Locate every Plasmodium parasite and identify its life-cycle stage.
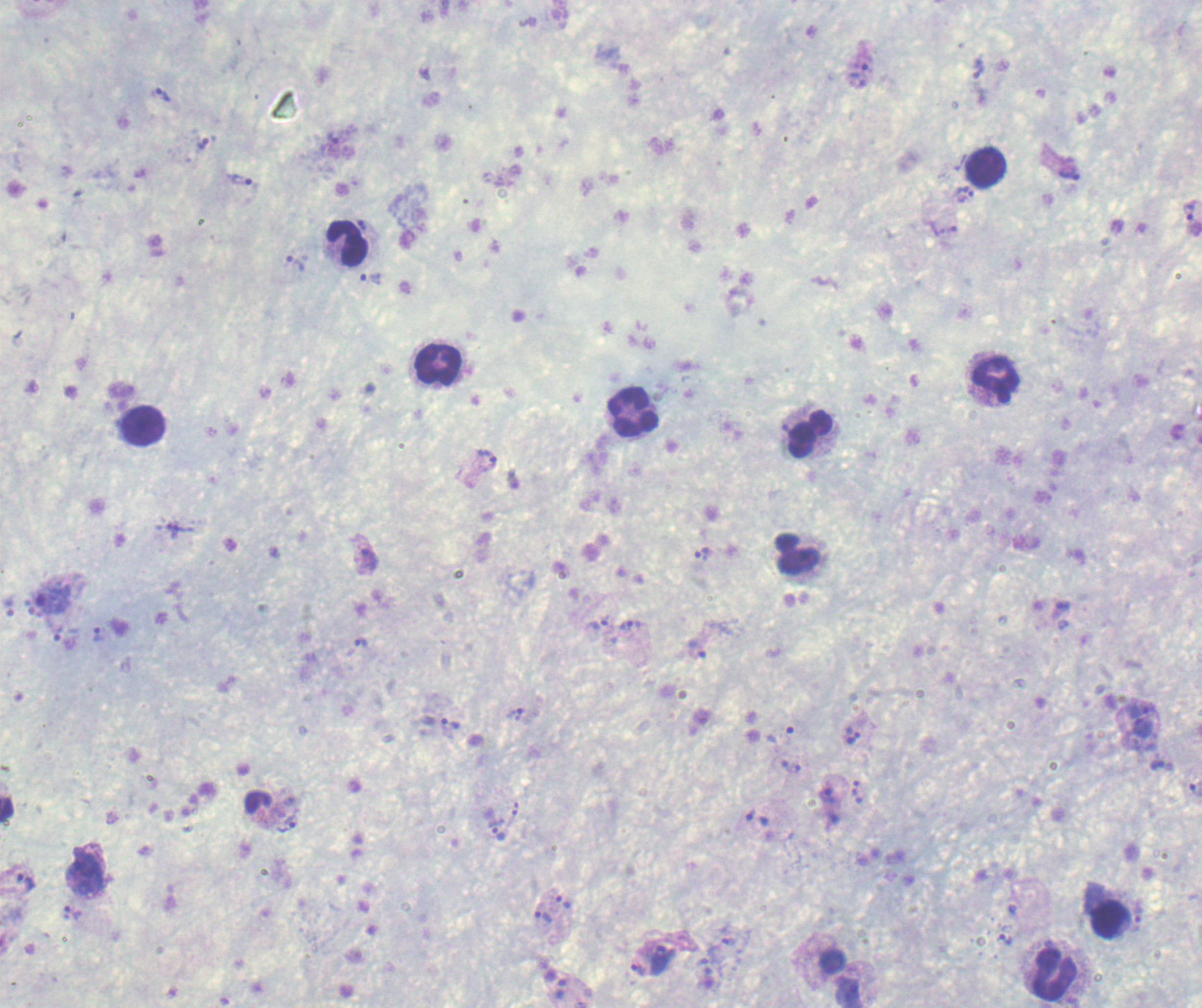

Approximate centers as (x, y) in pixels.
Trophozoites: (979, 68), (857, 75), (163, 95), (333, 137), (202, 144), (1069, 173), (240, 178), (964, 192), (1189, 212), (943, 228), (296, 263), (371, 278), (486, 461), (172, 529), (702, 552), (366, 561), (1061, 610), (598, 624), (627, 627), (99, 634), (360, 642), (697, 649), (1140, 710), (515, 714), (451, 724), (1141, 728), (852, 734), (780, 735), (1157, 764), (791, 766), (1195, 790), (858, 791), (827, 795), (515, 808), (750, 814), (287, 824), (496, 829), (83, 871), (26, 882), (563, 902), (72, 913), (542, 916), (1138, 919), (1006, 939), (730, 941), (658, 960), (638, 969), (560, 988), (847, 991).
No schizont or gametocyte forms observed.

Approximate centers as (x, y) in pixels.
Summary:
  - Leukocyte locations: (986, 168), (348, 244), (438, 362), (994, 378), (632, 411), (143, 427), (809, 433), (798, 553), (1108, 920), (1053, 974)
  - Field of view: single
  - Stain: Romanowsky
  - Background quality: poor
  - Magnification: 100x
  - Preparation: thick blood smear
  - Context: previously used in a real diagnosis
  - Image size: 1202×1008 pixels